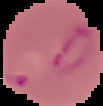
Image is 103×106 pixels. Result: Plasmodium parasites detected. From a thin blood film. Cell region segmented out of the field of view; the surrounding area is masked to black.